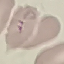
Summary:
  - Malaria status: uninfected
  - Stain: Giemsa
  - Preparation: thin blood film
  - Image type: cell patch, automatically extracted from a larger field of view and resized to 64 × 64 pixels
  - Capture: smartphone camera at the microscope eyepiece